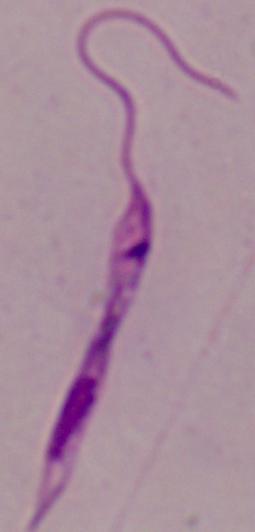

Summary:
  - Identification: Leishmania
  - Magnification: 1000x
  - Modality: photomicrograph